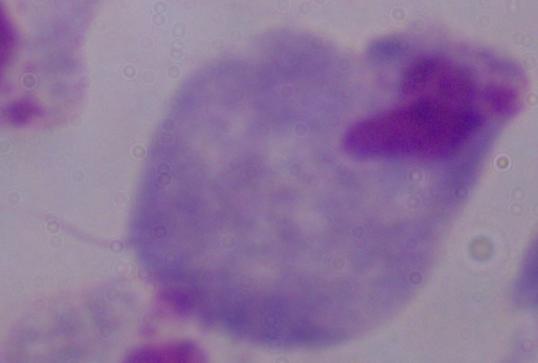
Summary:
  - Magnification: 1000x
  - Modality: photomicrograph
  - Identification: trichomonad